Comment on the morphology of the erythrocytes.
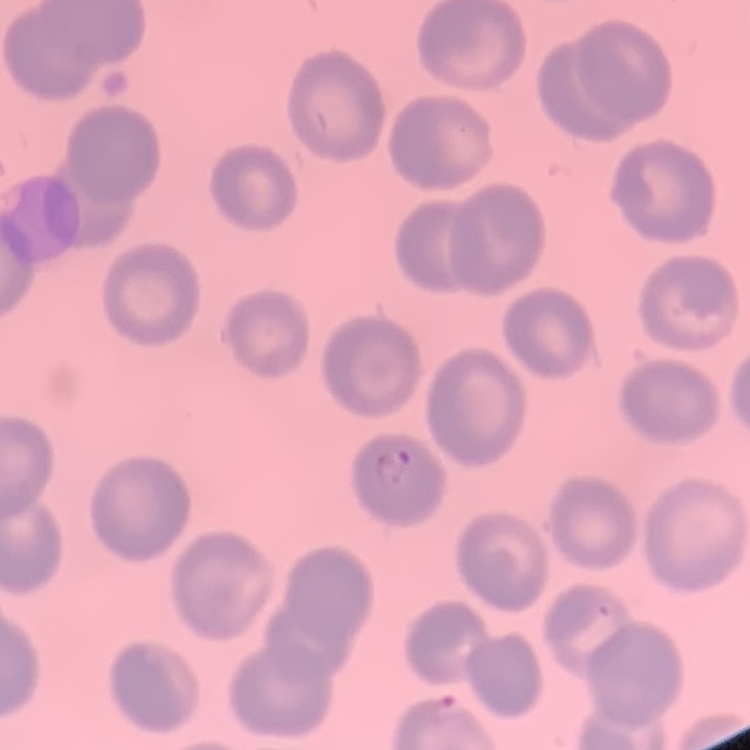
No rouleaux formation.

{
  "preparation": "thin blood smear",
  "stain": "Field's or Giemsa",
  "image_type": "one tile cut from a larger photomicrograph"
}